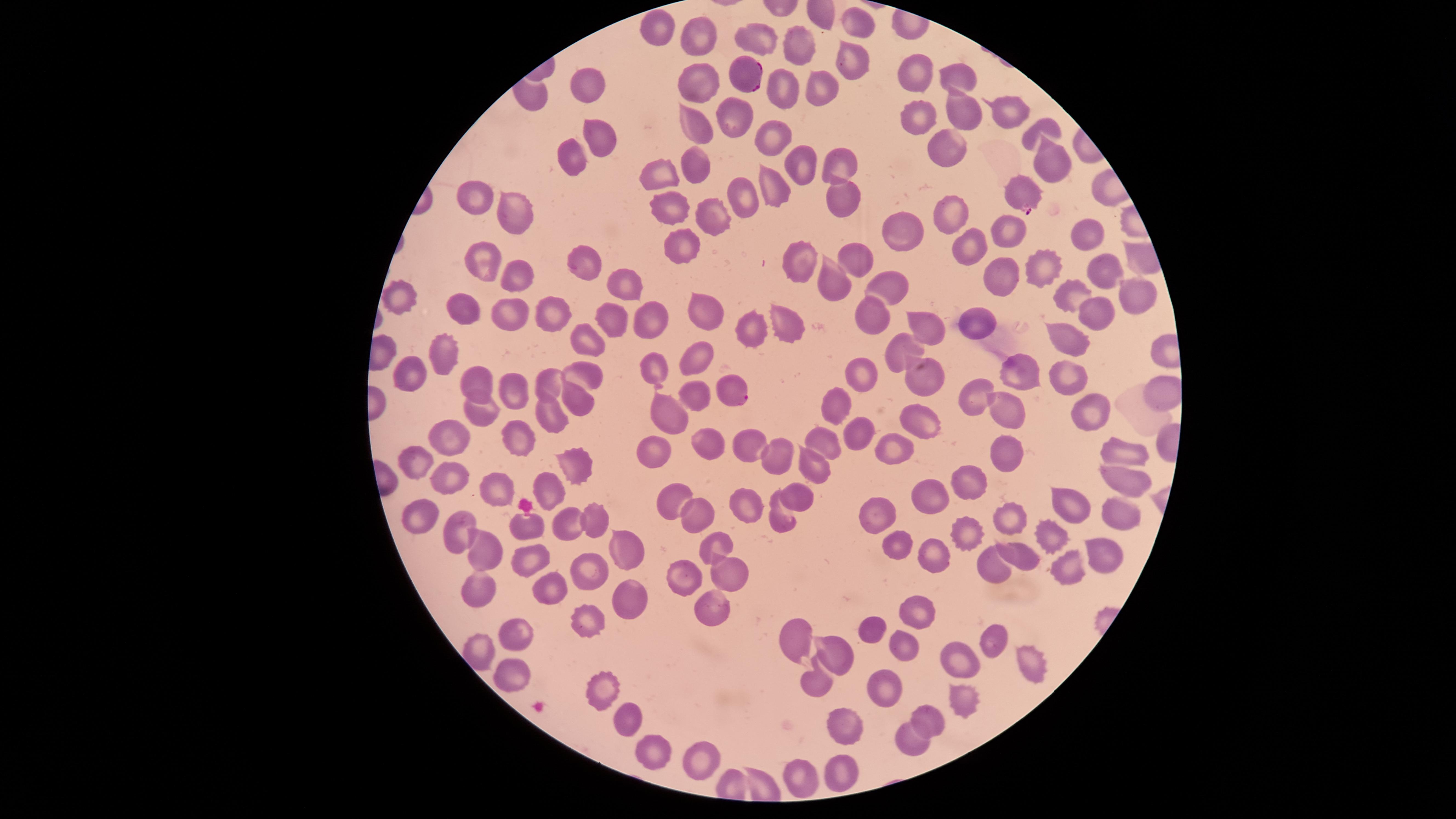

field of view = single
parasitized red blood cells = approximate marker points as [x, y] in pixels: [743, 73], [1018, 192], [729, 387]
stain = Giemsa
preparation = thin blood film
visible region = circular
capture = smartphone photograph through the microscope eyepiece
uninfected red blood cells = approximate marker points as [x, y] in pixels: [857, 24], [652, 28], [757, 33], [700, 35], [799, 41], [855, 59], [915, 73], [959, 77], [702, 84], [819, 84], [781, 85], [593, 87], [961, 111], [1006, 112], [920, 118], [733, 122], [697, 124], [1043, 129], [772, 130], [602, 136], [943, 145], [572, 158], [698, 159], [834, 162], [1045, 164], [800, 166], [659, 171], [774, 185], [477, 188], [841, 193], [743, 200], [669, 201], [515, 211], [708, 216], [951, 218], [904, 228], [1006, 229], [1080, 231], [677, 239], [967, 241], [852, 252], [580, 259], [797, 259], [483, 264], [1043, 269], [512, 273], [1001, 273], [1101, 273], [834, 275], [623, 281], [896, 284], [1066, 294], [1123, 295], [400, 301], [702, 309], [462, 310], [1091, 314], [547, 315], [511, 316], [873, 319], [610, 320], [650, 321], [969, 321], [926, 326], [784, 327], [750, 329], [1062, 331], [593, 340], [904, 350], [444, 354], [697, 356], [652, 369], [862, 371], [586, 372], [409, 375], [1068, 375], [1017, 376], [926, 379], [546, 384], [481, 387], [508, 390], [1161, 391], [973, 393], [689, 396], [581, 398], [833, 406], [1006, 407], [1091, 411], [549, 413], [483, 414], [920, 419], [658, 423], [852, 429], [515, 437], [444, 439], [746, 440], [710, 441], [818, 444], [895, 446], [1002, 451], [650, 452], [1116, 452], [781, 453], [577, 462], [418, 465], [809, 473], [972, 474], [449, 479], [498, 482], [1112, 482], [550, 490], [922, 491], [795, 492], [674, 499], [1072, 502], [745, 505], [698, 514], [1115, 514], [878, 515], [591, 517], [776, 519], [525, 521], [420, 522], [1011, 522], [569, 526], [965, 526], [458, 532], [1045, 537], [626, 545], [895, 546], [716, 547], [486, 548], [1011, 553], [929, 555], [527, 557], [1103, 558], [1064, 566], [585, 567], [988, 567], [682, 570], [729, 571], [478, 584], [550, 585], [630, 587], [710, 605], [585, 612], [915, 618], [870, 625], [791, 628], [514, 633], [904, 641], [989, 641], [484, 649], [835, 653], [1029, 656], [960, 661], [511, 676], [809, 679], [600, 682], [879, 687], [957, 705], [927, 712], [631, 713], [843, 721], [909, 741], [647, 750], [701, 755], [843, 766], [806, 774]
species = Plasmodium falciparum
image size = 1456×819 pixels
presence = malaria parasites detected